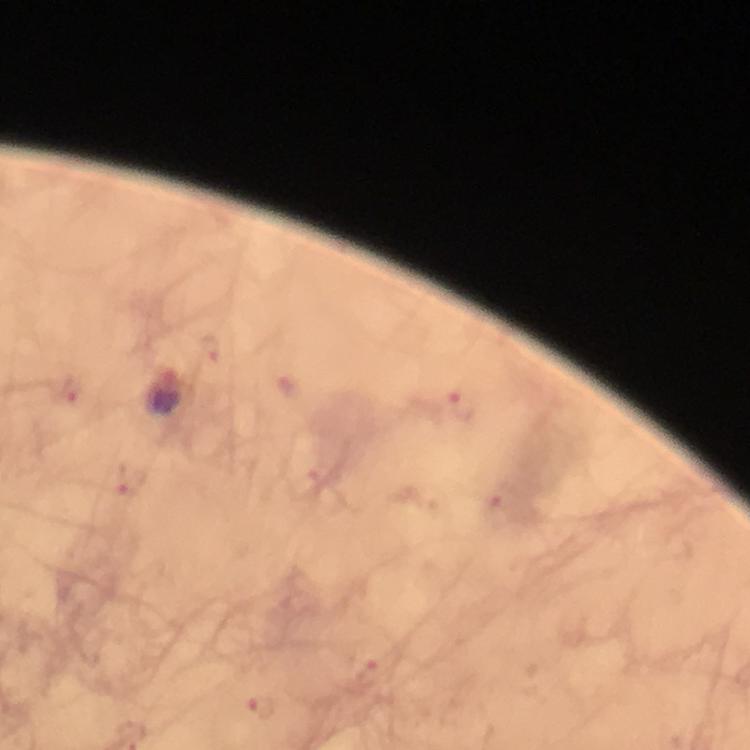

cropped from = a single field of view
immersion oil = applied
preparation = thick blood smear
magnification = 100x
Plasmodium parasite locations = approximate centers as {x, y} in pixels: {208, 348}, {287, 384}, {68, 389}, {460, 405}, {131, 480}, {497, 508}, {369, 673}, {261, 708}
capture = smartphone mounted on the microscope
image size = 750×750 pixels
context = from a diagnostic examination for malaria
stain = Giemsa